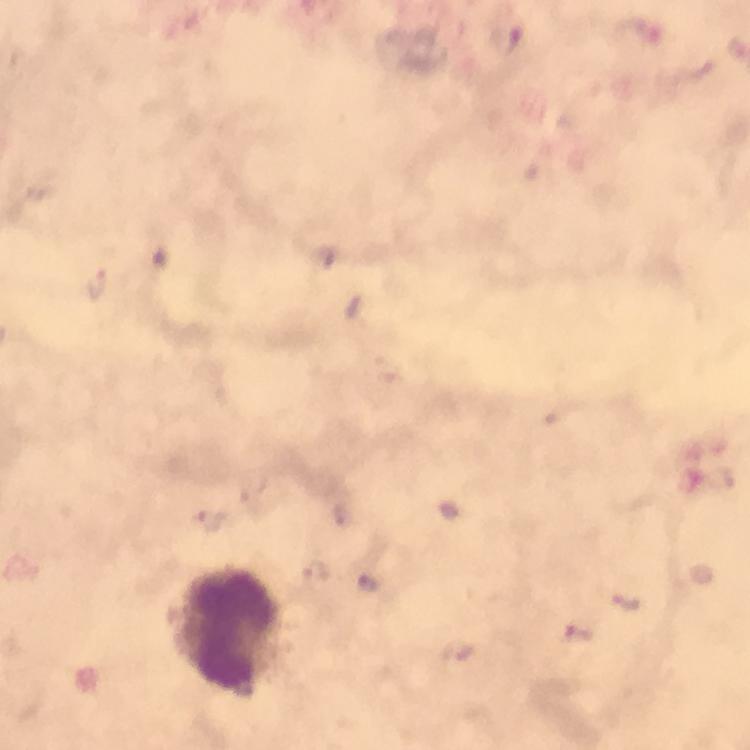
Approximate centers as {x, y} in pixels. Leukocyte locations: {223, 631}. Malaria parasite locations: {508, 39}, {324, 257}, {95, 285}, {448, 509}, {342, 515}, {208, 521}, {316, 574}, {372, 580}, {628, 604}, {578, 635}, {457, 652}. Image is 750×750 pixels. Cropped region of a single field of view. Immersion oil applied. At 100x magnification. Giemsa stain. Thick smear. Photographed with a smartphone mounted on the microscope. From a diagnostic examination for malaria.